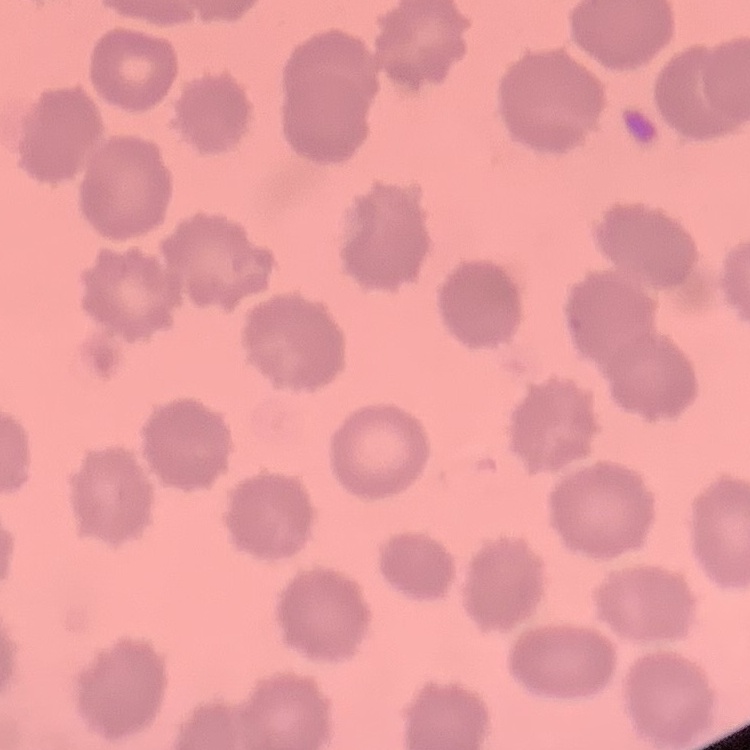

Summary:
  - Erythrocyte morphology: no rouleaux formation
  - Stain: Field's or Giemsa
  - Preparation: thin blood film
  - Image type: square crop of a larger photomicrograph